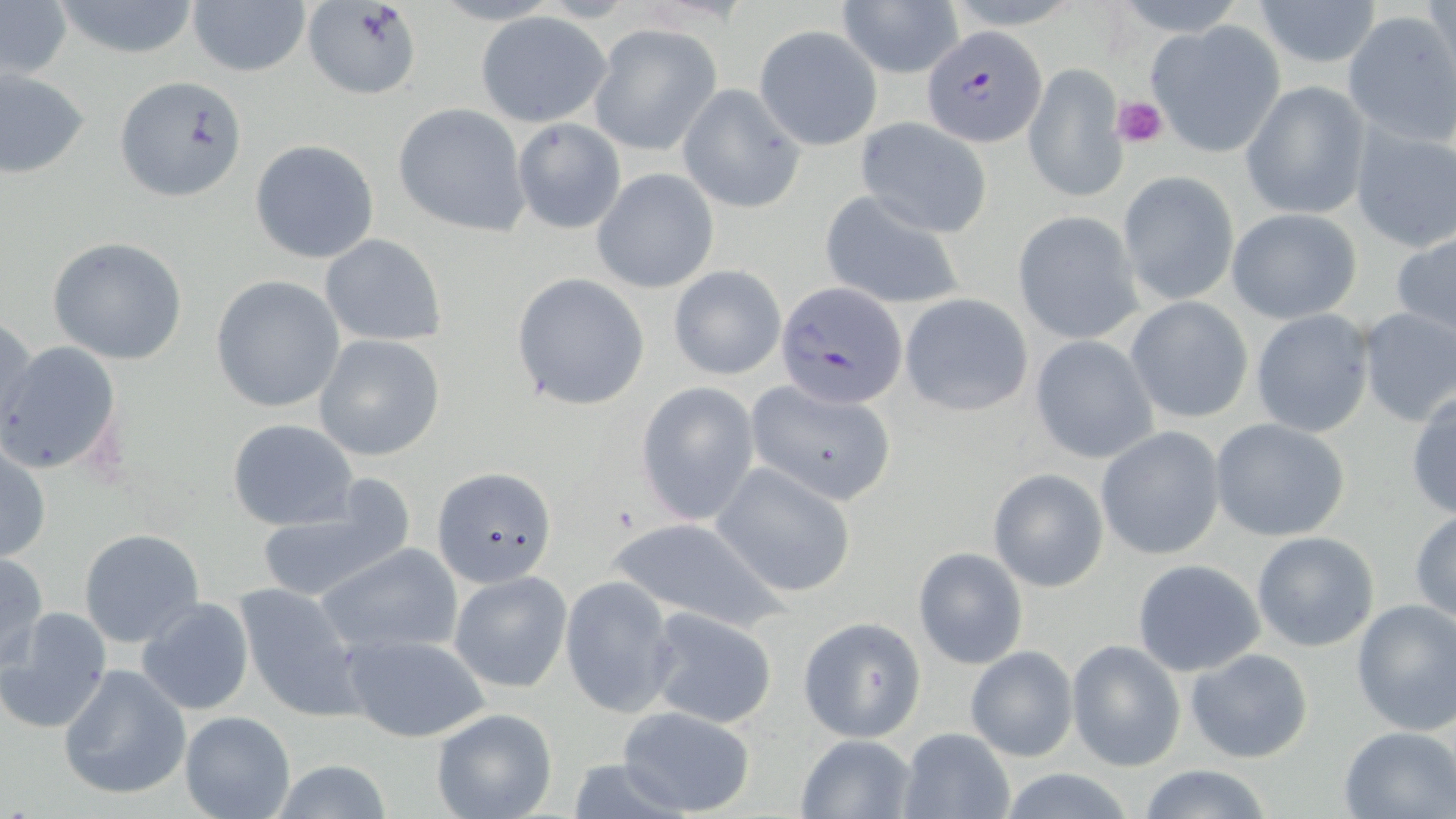

Plasmodium falciparum-infected red blood cell locations = approximate bounding boxes as [x1, y1, x2, y2] in pixels: [923, 27, 1046, 147], [778, 281, 909, 405]
slide-level diagnosis = Plasmodium falciparum
uninfected red blood cell locations = approximate bounding boxes as [x1, y1, x2, y2] in pixels: [50, 0, 205, 60], [1252, 0, 1384, 70], [185, 1, 311, 80], [839, 1, 962, 78], [0, 2, 71, 82], [302, 2, 424, 100], [1343, 10, 1456, 145], [475, 11, 611, 126], [1145, 19, 1285, 158], [590, 24, 721, 154], [754, 24, 882, 152], [1023, 62, 1127, 203], [0, 67, 90, 178], [114, 74, 249, 202], [1242, 79, 1371, 217], [678, 84, 804, 213], [393, 103, 531, 236], [854, 117, 992, 238], [511, 118, 626, 234], [1350, 123, 1456, 252], [250, 139, 377, 264], [592, 168, 718, 292], [1118, 170, 1238, 305], [819, 191, 967, 311], [1226, 207, 1362, 323], [1015, 210, 1142, 343], [1390, 229, 1456, 339], [321, 233, 446, 345], [45, 236, 191, 366], [668, 266, 786, 381], [512, 273, 650, 410], [211, 274, 345, 413], [900, 292, 1033, 415], [1125, 297, 1254, 424], [1354, 306, 1456, 428], [1249, 309, 1374, 436], [1, 313, 39, 436], [312, 334, 447, 462], [1030, 335, 1158, 464], [0, 339, 124, 477], [745, 381, 898, 505], [636, 382, 760, 527], [1407, 388, 1456, 520], [228, 417, 358, 530], [1210, 417, 1352, 542], [1096, 427, 1226, 560], [0, 442, 50, 565], [711, 462, 858, 597], [433, 465, 555, 587], [988, 468, 1108, 591], [255, 481, 412, 608], [1410, 508, 1456, 626], [608, 516, 785, 632], [77, 528, 205, 649], [1252, 531, 1380, 652], [315, 543, 464, 658], [913, 547, 1028, 670], [0, 551, 48, 676], [1132, 558, 1267, 678], [450, 570, 572, 693], [561, 575, 677, 718], [232, 582, 365, 720], [135, 598, 255, 716], [1351, 599, 1456, 735], [0, 606, 111, 735], [642, 607, 780, 729], [798, 617, 926, 742], [341, 634, 489, 743], [1068, 640, 1186, 770], [965, 646, 1079, 762], [1185, 647, 1315, 764], [57, 662, 191, 800], [614, 703, 758, 817], [429, 707, 558, 819], [180, 711, 296, 819], [897, 726, 1017, 819], [1340, 727, 1456, 817], [796, 734, 916, 818], [266, 758, 398, 819], [1135, 764, 1279, 819], [994, 766, 1144, 819]
magnification = 1000x
preparation = thin blood smear
modality = light microscopy
platelet locations = approximate bounding boxes as [x1, y1, x2, y2] in pixels: [1112, 94, 1169, 148]
field of view = single
stain = May-Grünwald-Giemsa
image size = 1456×819 pixels